Name the parasite shown.
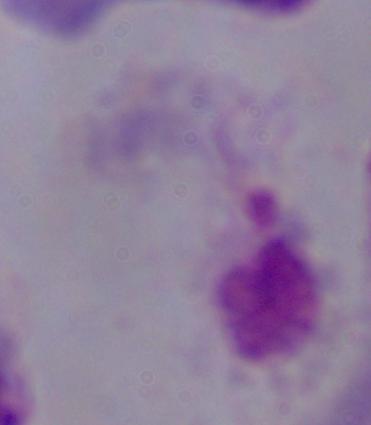

This is a trichomonad.

Photomicrograph. Captured at 1000x magnification.